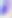

Summary:
  - Modality: photomicrograph
  - Magnification: 400x
  - Identification: Toxoplasma gondii